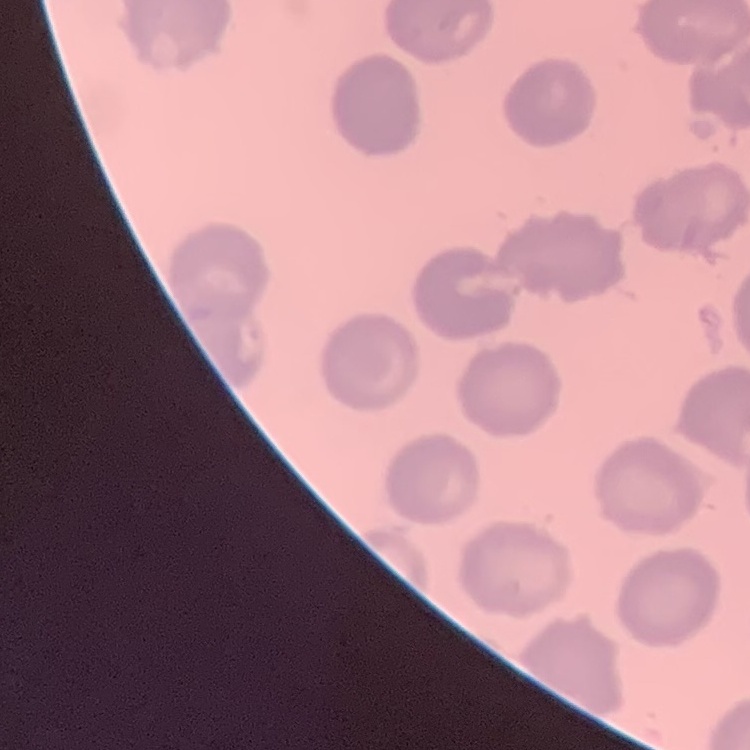 The erythrocytes show no rouleaux formation. Field's or Giemsa stain. Thin blood smear. One tile cut from a larger photomicrograph.